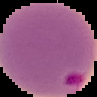

Image is 97×97 pixels. Cell region segmented out of the field of view; the surrounding area is masked to black. Result: Plasmodium parasites detected. From a thin blood film.